Identify the parasite.
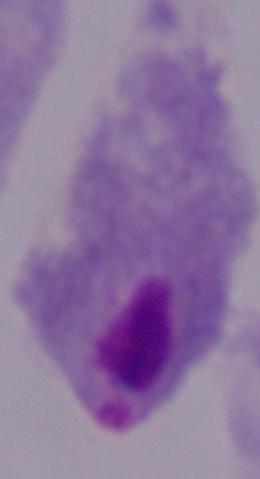
This is a trichomonad.

Photomicrograph. Captured at 1000x magnification.